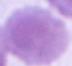
Summary:
  - Modality: photomicrograph
  - Identification: erythrocyte
  - Magnification: 1000x